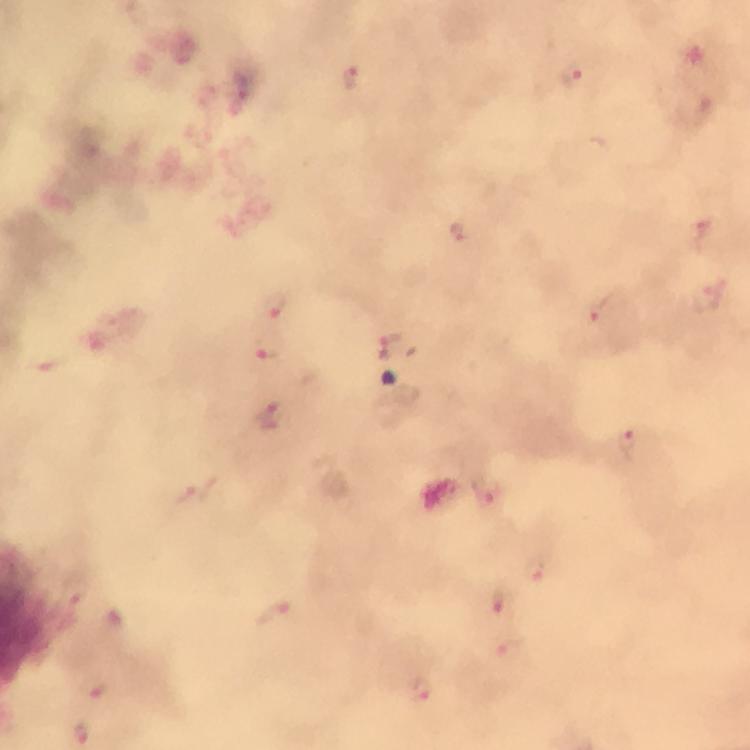 Approximate centers as {x, y} in pixels. Plasmodium parasite locations: {572, 77}, {351, 78}, {457, 232}, {708, 299}, {274, 305}, {597, 308}, {389, 338}, {267, 346}, {272, 416}, {628, 441}, {486, 493}, {533, 569}, {497, 601}, {273, 612}, {93, 686}, {418, 688}, {83, 733}. 100x magnification. Smartphone photograph taken through a microscope. Giemsa-stained preparation. Cropped region of a single field of view. Thick smear. Immersion oil applied. Image is 750×750 pixels. From a malaria diagnostic workup.